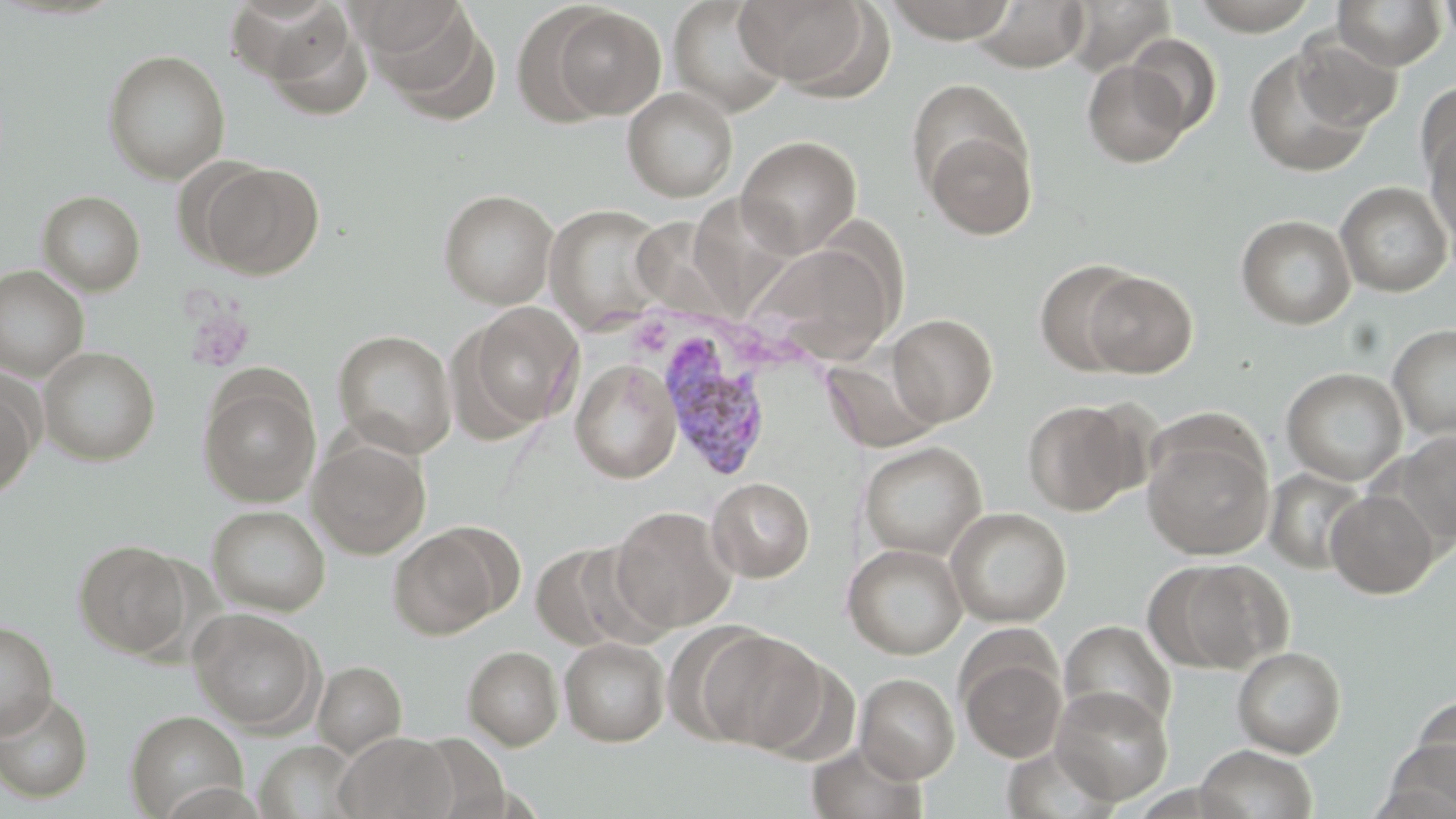

slide_level_diagnosis: Plasmodium vivax
platelet_locations: 'approximate bounding boxes as (x1, y1, x2, y2) in pixels: (182, 303, 254, 373)'
stain: May-Grünwald-Giemsa
magnification: 1000x
uninfected_red_blood_cell_locations: 'approximate bounding boxes as (x1, y1, x2, y2) in pixels: (668, 0, 790, 116), (735, 0, 877, 91), (883, 0, 1019, 43), (1187, 0, 1322, 34), (1439, 0, 1456, 50), (1065, 1, 1175, 76), (1333, 1, 1447, 70), (363, 2, 495, 116), (972, 2, 1091, 73), (545, 6, 667, 121), (258, 11, 372, 120), (1126, 33, 1222, 137), (1292, 33, 1403, 134), (1243, 46, 1376, 179), (103, 49, 230, 183), (1082, 58, 1193, 167), (1415, 80, 1456, 186), (622, 87, 738, 201), (1424, 124, 1456, 249), (922, 125, 1037, 239), (736, 135, 862, 257), (198, 160, 324, 279), (1335, 182, 1454, 297), (438, 189, 558, 309), (37, 190, 145, 295), (545, 204, 671, 335), (1236, 214, 1357, 330), (747, 241, 900, 365), (1034, 259, 1146, 376), (0, 265, 89, 381), (1083, 271, 1197, 377), (460, 302, 583, 431), (888, 313, 998, 426), (1388, 323, 1456, 440), (333, 330, 457, 458), (39, 347, 160, 465), (820, 354, 940, 453), (571, 359, 682, 483), (1281, 367, 1408, 485), (198, 374, 321, 507), (0, 377, 40, 497), (1022, 399, 1140, 515), (1142, 430, 1274, 560), (1391, 430, 1456, 546), (308, 437, 431, 559), (859, 442, 987, 560), (1264, 467, 1370, 574), (708, 477, 814, 582), (1325, 489, 1438, 598), (207, 505, 330, 616), (610, 505, 737, 633), (945, 507, 1072, 627), (388, 525, 507, 639), (74, 540, 192, 658), (531, 542, 640, 651), (843, 543, 967, 659), (1157, 558, 1291, 673), (189, 607, 323, 734), (1059, 620, 1176, 733), (0, 621, 58, 739), (695, 627, 829, 754), (559, 637, 670, 746), (463, 646, 563, 750), (1232, 646, 1347, 758), (958, 650, 1067, 762), (312, 660, 406, 759), (855, 673, 959, 783), (1051, 686, 1174, 805), (0, 691, 94, 803), (1410, 695, 1456, 796), (125, 709, 248, 819), (335, 732, 457, 819), (403, 735, 511, 818), (806, 740, 928, 819), (254, 741, 363, 819), (1001, 741, 1118, 819), (1377, 741, 1456, 817), (1194, 744, 1318, 819)'
plasmodium_vivax_infected_red_blood_cell_locations: 'approximate bounding boxes as (x1, y1, x2, y2) in pixels: (655, 327, 774, 483)'
image_size: 1456×819 pixels
preparation: thin blood smear
field_of_view: one of a larger specimen
modality: optical microscopy